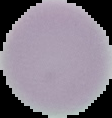
Summary:
  - Image size: 112×118 pixels
  - Result: no malaria parasites detected
  - Preparation: thin blood film
  - Image type: segmented cell region on a black background